Draw a bounding box around every Plasmodium parasite.
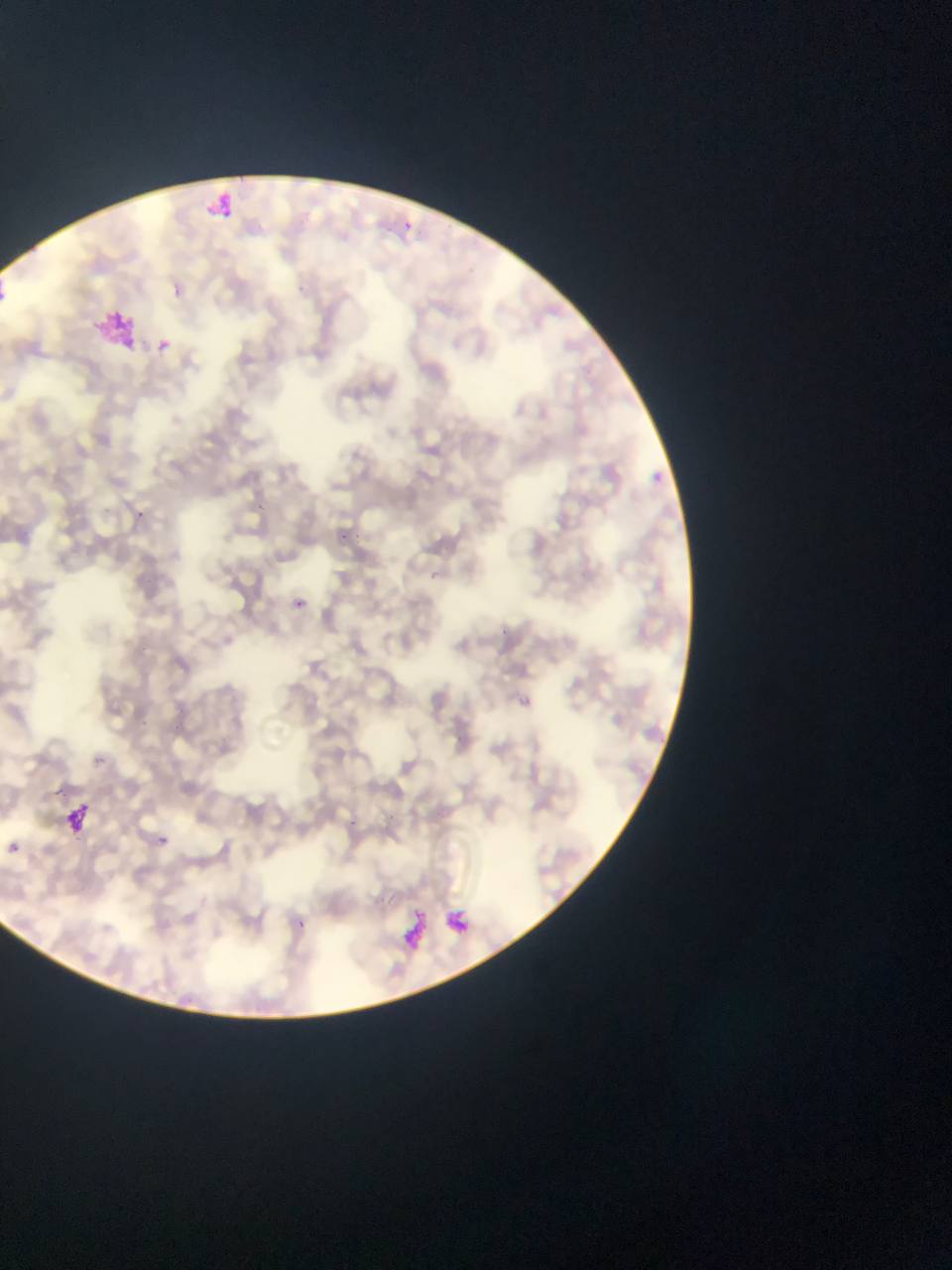
Approximate bounding boxes as (left, top, right, bottom) in pixels.
Plasmodium parasites: (391, 213, 421, 239), (157, 339, 170, 352), (646, 464, 683, 503), (293, 593, 318, 613), (518, 696, 531, 709), (151, 823, 176, 854), (9, 842, 20, 852), (291, 910, 310, 932).

Summary:
  - Artifact (stain precipitate or debris) locations: (203, 183, 234, 222), (96, 309, 137, 355), (58, 791, 97, 831), (446, 900, 496, 937), (402, 916, 430, 952)
  - Capture: mobile-phone photograph through a microscope
  - Country: Ghana
  - Preparation: thin blood smear
  - Field of view: single
  - Image size: 952×1270 pixels